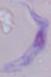

Summary:
  - Modality: photomicrograph
  - Magnification: 1000x
  - Identification: trypanosome